Comment on the morphology of the erythrocytes.
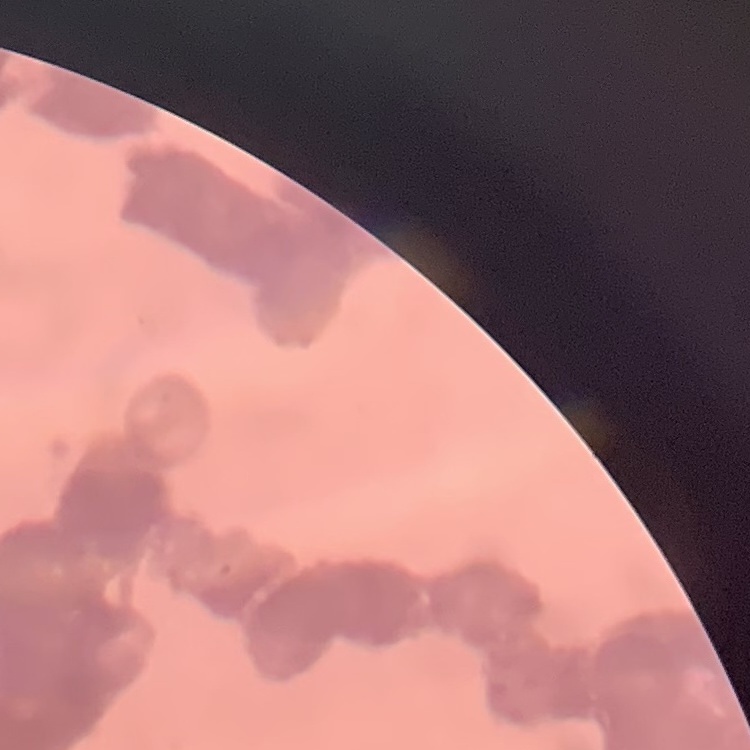
They show rouleaux formation.

stain = Field's or Giemsa
preparation = thin blood film
image type = one tile cut from a larger photomicrograph